Assess this cell for malaria.
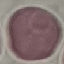
It is uninfected.

Thin smear of blood. Acquired by smartphone through the microscope eyepiece. Giemsa-stained preparation. Automatically extracted cell patch, resized to 64 × 64 pixels.